Classify this cell by malaria status.
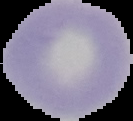

Uninfected.

Cell region segmented out of the field of view; the surrounding area is masked to black. From a thin blood film. Image is 133×121 pixels.